State which parasite is depicted.
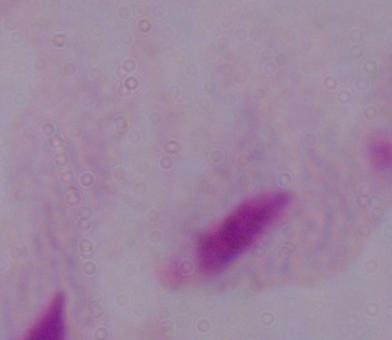
This is a trichomonad.

Summary:
  - Modality: photomicrograph
  - Magnification: 1000x